Outline each uninfected red blood cell.
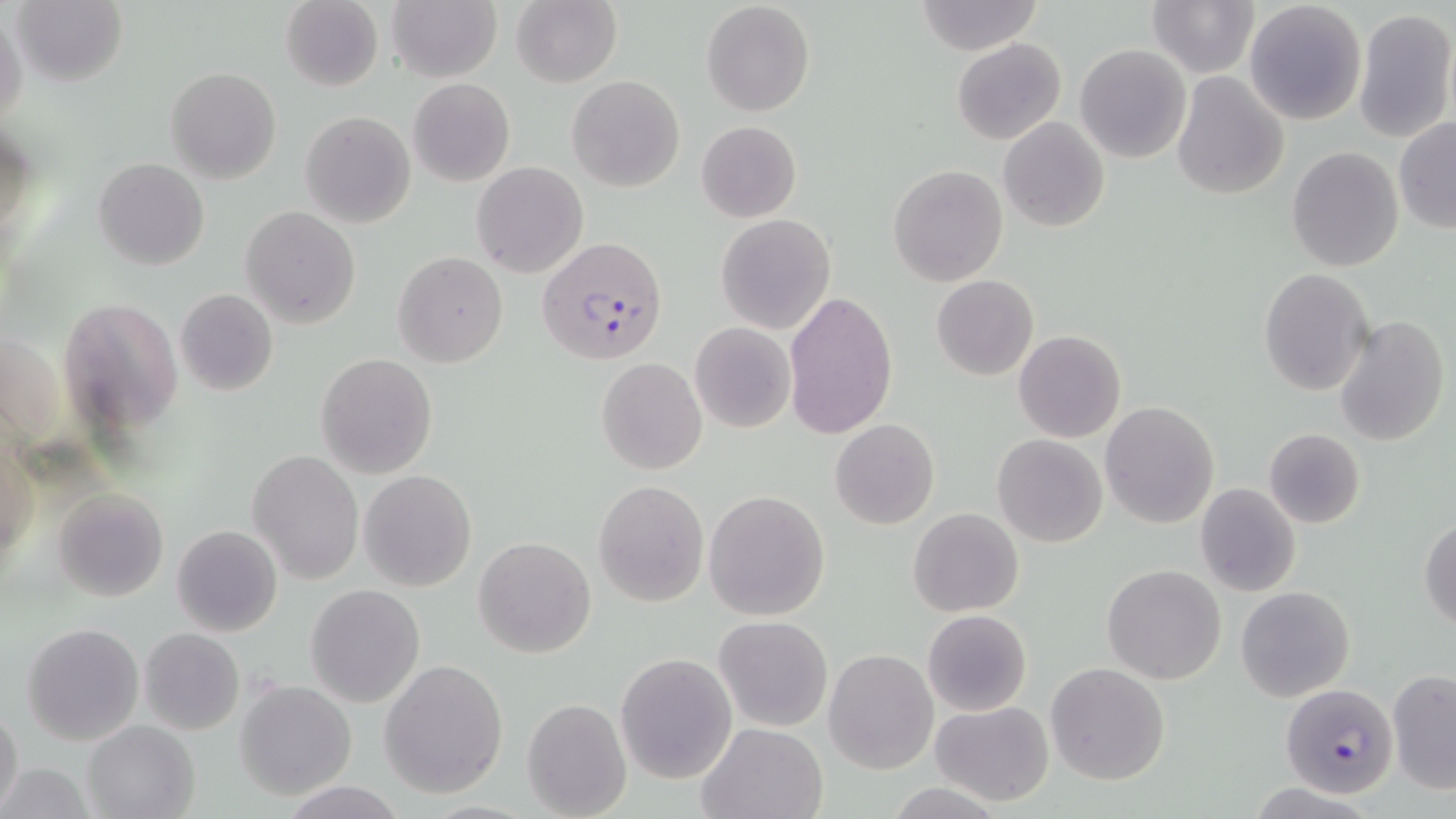
Approximate bounding boxes as named x1/y1/x2/y2 corners in pixels.
Uninfected red blood cells: (x1=12, y1=0, x2=127, y2=86), (x1=280, y1=0, x2=384, y2=91), (x1=1146, y1=0, x2=1258, y2=78), (x1=1243, y1=0, x2=1368, y2=124), (x1=388, y1=1, x2=500, y2=82), (x1=511, y1=1, x2=622, y2=87), (x1=702, y1=1, x2=815, y2=115), (x1=914, y1=1, x2=1042, y2=53), (x1=1355, y1=7, x2=1455, y2=142), (x1=0, y1=8, x2=27, y2=131), (x1=952, y1=37, x2=1066, y2=144), (x1=1075, y1=45, x2=1192, y2=164), (x1=165, y1=66, x2=281, y2=184), (x1=1172, y1=72, x2=1289, y2=199), (x1=567, y1=75, x2=686, y2=192), (x1=408, y1=77, x2=514, y2=186), (x1=300, y1=111, x2=416, y2=227), (x1=998, y1=116, x2=1110, y2=233), (x1=1394, y1=119, x2=1456, y2=234), (x1=696, y1=121, x2=802, y2=222), (x1=1, y1=123, x2=39, y2=242), (x1=1286, y1=147, x2=1404, y2=272), (x1=94, y1=158, x2=208, y2=271), (x1=471, y1=162, x2=589, y2=279), (x1=887, y1=164, x2=1009, y2=286), (x1=240, y1=206, x2=360, y2=328), (x1=715, y1=213, x2=835, y2=334), (x1=393, y1=251, x2=508, y2=367), (x1=1258, y1=268, x2=1374, y2=395), (x1=932, y1=275, x2=1039, y2=381), (x1=176, y1=289, x2=278, y2=396), (x1=784, y1=289, x2=899, y2=440), (x1=59, y1=293, x2=182, y2=435), (x1=1334, y1=316, x2=1450, y2=448), (x1=690, y1=322, x2=795, y2=433), (x1=1012, y1=329, x2=1126, y2=443), (x1=316, y1=353, x2=437, y2=478), (x1=596, y1=357, x2=707, y2=474), (x1=1100, y1=401, x2=1219, y2=530), (x1=831, y1=418, x2=939, y2=529), (x1=1263, y1=428, x2=1366, y2=529), (x1=992, y1=434, x2=1108, y2=547), (x1=248, y1=449, x2=362, y2=584), (x1=360, y1=469, x2=478, y2=592), (x1=592, y1=479, x2=709, y2=608), (x1=1194, y1=484, x2=1302, y2=598), (x1=54, y1=487, x2=168, y2=603), (x1=704, y1=491, x2=830, y2=621), (x1=908, y1=506, x2=1025, y2=617), (x1=1419, y1=515, x2=1456, y2=631), (x1=172, y1=524, x2=283, y2=637), (x1=474, y1=537, x2=596, y2=658), (x1=1101, y1=564, x2=1227, y2=685), (x1=305, y1=584, x2=426, y2=708), (x1=1235, y1=585, x2=1356, y2=703), (x1=922, y1=609, x2=1033, y2=717), (x1=714, y1=616, x2=832, y2=732), (x1=22, y1=623, x2=144, y2=747), (x1=139, y1=628, x2=244, y2=735), (x1=825, y1=649, x2=937, y2=772), (x1=615, y1=653, x2=736, y2=785), (x1=379, y1=658, x2=509, y2=797), (x1=1046, y1=663, x2=1169, y2=786), (x1=1388, y1=669, x2=1456, y2=792), (x1=235, y1=680, x2=357, y2=801), (x1=522, y1=697, x2=631, y2=818), (x1=928, y1=700, x2=1055, y2=805), (x1=0, y1=706, x2=24, y2=814), (x1=81, y1=720, x2=200, y2=818), (x1=695, y1=721, x2=828, y2=819), (x1=0, y1=763, x2=93, y2=819), (x1=279, y1=780, x2=408, y2=817).

slide_level_diagnosis: Plasmodium falciparum
preparation: thin blood smear
plasmodium_falciparum_infected_red_blood_cell_locations: 'approximate bounding boxes as named x1/y1/x2/y2 corners in pixels: (x1=537, y1=238, x2=668, y2=368), (x1=1280, y1=684, x2=1398, y2=798)'
stain: May-Grünwald-Giemsa
image_size: 1456×819 pixels
magnification: 1000x
field_of_view: one of a larger specimen
modality: light microscopy